Report the malaria status of this cell.
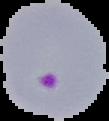

It is parasitized.

image size = 109×121 pixels
preparation = thin blood smear
image type = segmented cell region on a black background